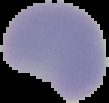 Segmented cell region on a black background. Image is 109×103 pixels. Result: negative for Plasmodium parasites. From a thin blood film.